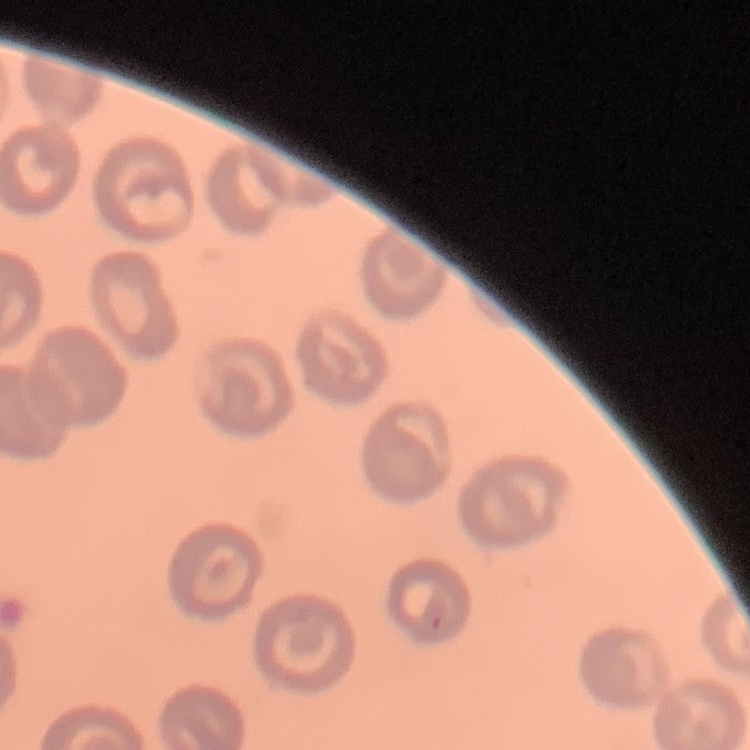 The red blood cells exhibit no rouleaux formation. Stained with either Field's or Giemsa. Square crop of a larger photomicrograph. Thin peripheral smear.